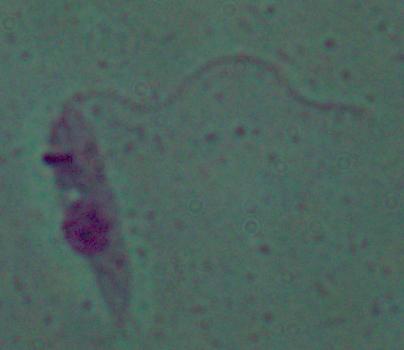
Summary:
  - Magnification: 1000x
  - Identification: Leishmania
  - Modality: photomicrograph